Point out each Plasmodium parasite.
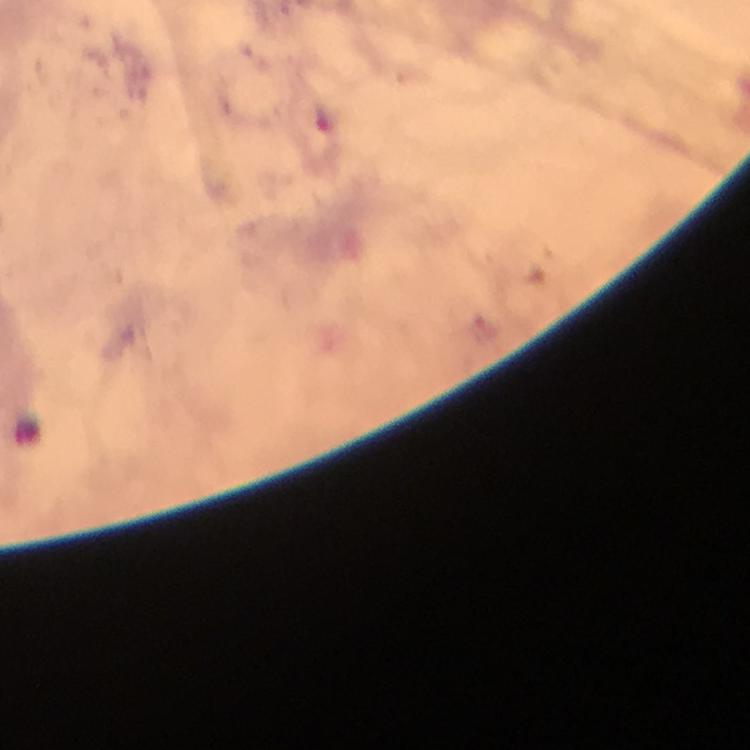
Approximate centers as (x, y) in pixels.
Plasmodium parasites: (488, 330).

capture = smartphone camera through the microscope
cropped from = one field of view
image size = 750×750 pixels
context = from a malaria diagnostic workup
magnification = 100x
immersion oil = used
preparation = thick smear
stain = Giemsa